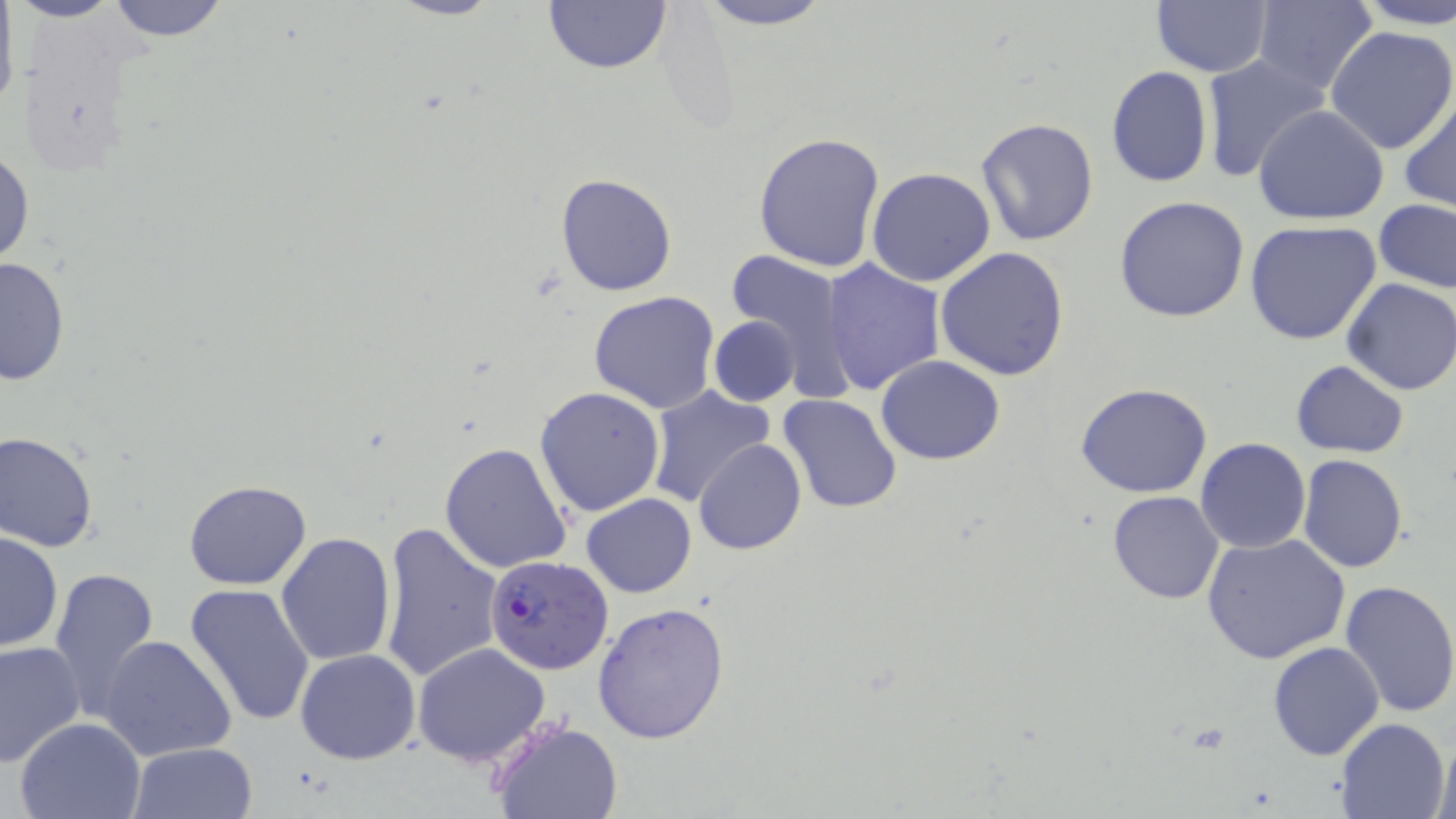
slide-level diagnosis = Plasmodium falciparum
preparation = thin blood film
magnification = 1000x
uninfected red blood cell locations = approximate bounding boxes as named x1/y1/x2/y2 corners in pixels: (x1=11, y1=0, x2=124, y2=23), (x1=101, y1=0, x2=231, y2=42), (x1=387, y1=0, x2=503, y2=22), (x1=541, y1=0, x2=674, y2=77), (x1=694, y1=0, x2=835, y2=29), (x1=1251, y1=0, x2=1379, y2=96), (x1=1348, y1=0, x2=1456, y2=30), (x1=1151, y1=1, x2=1272, y2=77), (x1=0, y1=11, x2=18, y2=120), (x1=1326, y1=25, x2=1456, y2=155), (x1=1200, y1=53, x2=1332, y2=183), (x1=1106, y1=66, x2=1213, y2=188), (x1=1399, y1=94, x2=1456, y2=214), (x1=1253, y1=105, x2=1389, y2=225), (x1=975, y1=117, x2=1101, y2=248), (x1=754, y1=131, x2=887, y2=271), (x1=0, y1=145, x2=35, y2=272), (x1=866, y1=167, x2=996, y2=287), (x1=555, y1=172, x2=677, y2=296), (x1=1115, y1=195, x2=1251, y2=322), (x1=1374, y1=200, x2=1456, y2=293), (x1=1244, y1=220, x2=1382, y2=345), (x1=721, y1=247, x2=857, y2=398), (x1=937, y1=247, x2=1070, y2=380), (x1=0, y1=256, x2=71, y2=386), (x1=819, y1=258, x2=946, y2=396), (x1=1341, y1=277, x2=1456, y2=395), (x1=588, y1=291, x2=721, y2=413), (x1=708, y1=315, x2=801, y2=407), (x1=876, y1=356, x2=1005, y2=465), (x1=1290, y1=359, x2=1409, y2=458), (x1=1075, y1=382, x2=1214, y2=498), (x1=644, y1=384, x2=776, y2=507), (x1=535, y1=386, x2=666, y2=517), (x1=779, y1=394, x2=904, y2=514), (x1=0, y1=429, x2=99, y2=551), (x1=1194, y1=438, x2=1310, y2=554), (x1=694, y1=440, x2=807, y2=555), (x1=439, y1=442, x2=573, y2=575), (x1=1298, y1=454, x2=1408, y2=573), (x1=183, y1=480, x2=313, y2=589), (x1=1107, y1=491, x2=1224, y2=605), (x1=582, y1=494, x2=697, y2=598), (x1=377, y1=518, x2=505, y2=686), (x1=0, y1=530, x2=62, y2=653), (x1=275, y1=532, x2=397, y2=668), (x1=1203, y1=533, x2=1351, y2=665), (x1=49, y1=564, x2=160, y2=724), (x1=1339, y1=578, x2=1456, y2=720), (x1=184, y1=584, x2=315, y2=728), (x1=593, y1=601, x2=730, y2=745), (x1=99, y1=637, x2=237, y2=760), (x1=0, y1=639, x2=85, y2=768), (x1=1268, y1=641, x2=1384, y2=760), (x1=411, y1=643, x2=554, y2=767), (x1=296, y1=649, x2=421, y2=765), (x1=13, y1=717, x2=148, y2=819), (x1=490, y1=717, x2=625, y2=818), (x1=1336, y1=717, x2=1453, y2=819), (x1=1431, y1=731, x2=1454, y2=819), (x1=127, y1=742, x2=258, y2=819)
image size = 1456×819 pixels
Plasmodium falciparum-infected red blood cell locations = approximate bounding boxes as named x1/y1/x2/y2 corners in pixels: (x1=486, y1=553, x2=613, y2=674)
field of view = one of a larger specimen
modality = light microscopy
stain = May-Grünwald-Giemsa